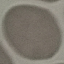

{
  "result": "no malaria parasites seen",
  "capture": "smartphone through the microscope eyepiece",
  "preparation": "thin blood film",
  "stain": "Giemsa",
  "image_type": "cell patch, automatically extracted from a larger field of view and resized to 64 × 64 pixels"
}